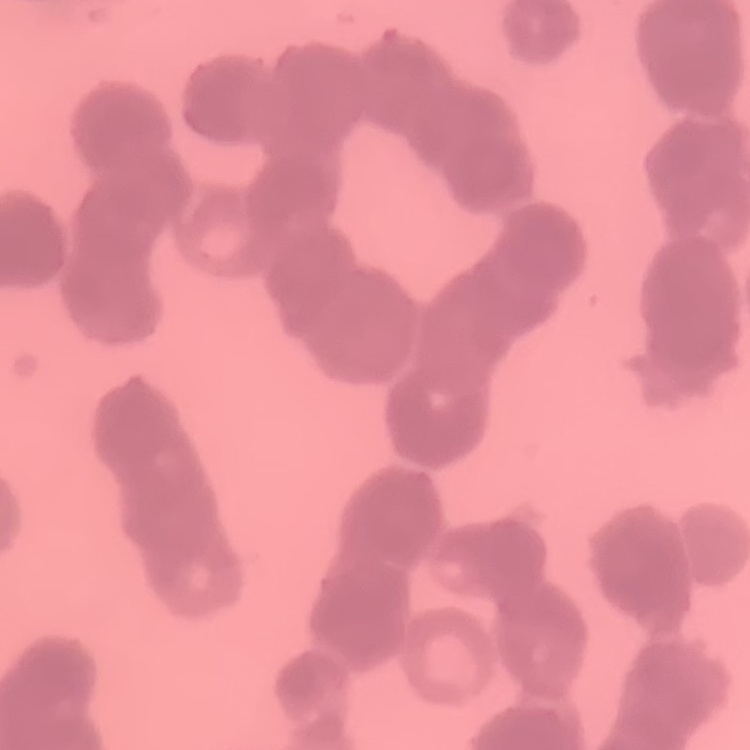

Summary:
  - Red blood cell morphology: rouleaux formation
  - Stain: Field's or Giemsa
  - Preparation: thin blood smear
  - Image type: square crop of a larger photomicrograph